State which parasite is depicted.
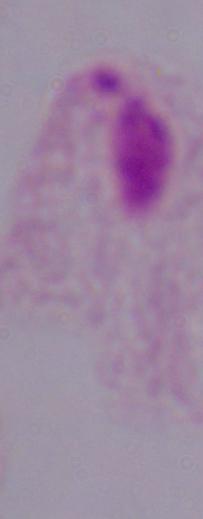

A trichomonad.

modality: micrograph
magnification: 1000x